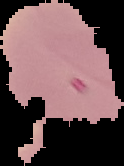

preparation = thin blood smear
image type = segmented cell region with the area outside set to black
result = negative for malaria parasites
image size = 124×166 pixels